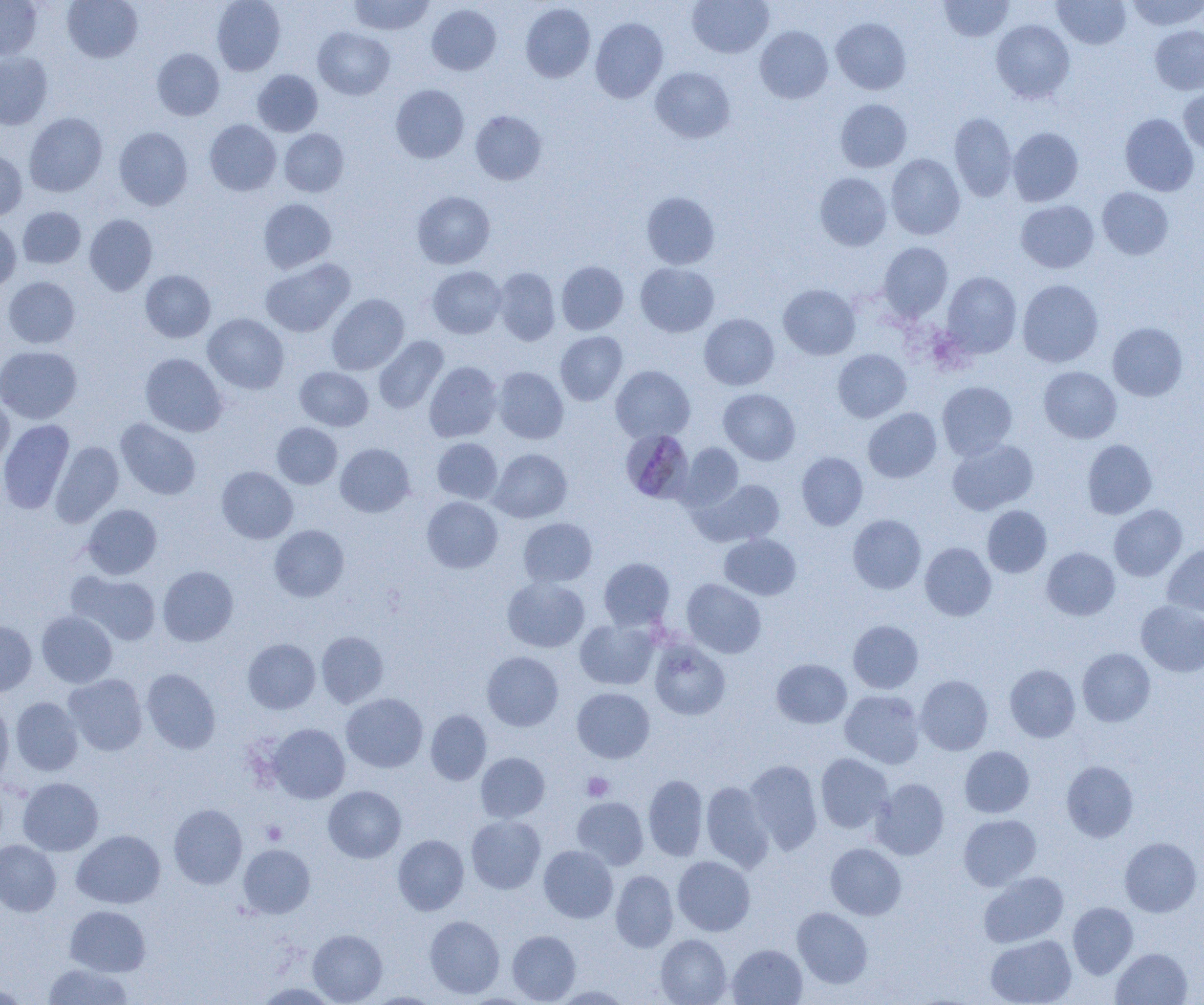

slide-level diagnosis = Plasmodium malariae
image size = 1204×1005 pixels
modality = optical microscopy
magnification = 1000x
Plasmodium malariae-infected red blood cell locations = approximate bounding boxes as [x1, y1, x2, y2] in pixels: [622, 430, 697, 502]
field of view = single
uninfected red blood cell locations = approximate bounding boxes as [x1, y1, x2, y2] in pixels: [0, 0, 42, 60], [62, 0, 142, 62], [212, 0, 286, 75], [348, 0, 434, 35], [687, 0, 773, 58], [939, 0, 1014, 42], [1053, 0, 1130, 49], [1126, 0, 1203, 32], [520, 3, 595, 83], [427, 4, 501, 76], [831, 17, 911, 94], [590, 18, 668, 103], [991, 19, 1075, 103], [755, 25, 833, 103], [1149, 25, 1204, 94], [313, 27, 394, 99], [152, 48, 224, 120], [0, 52, 53, 130], [650, 67, 735, 143], [252, 69, 323, 137], [390, 84, 469, 163], [1179, 87, 1204, 156], [835, 99, 912, 172], [470, 110, 546, 185], [24, 112, 107, 197], [949, 112, 1016, 201], [1120, 113, 1199, 196], [205, 119, 281, 196], [114, 127, 193, 210], [1008, 127, 1083, 206], [280, 129, 349, 197], [0, 150, 27, 221], [887, 153, 965, 240], [814, 172, 892, 250], [1097, 187, 1174, 260], [412, 191, 495, 269], [641, 192, 719, 269], [258, 198, 336, 273], [1016, 200, 1099, 273], [18, 207, 85, 268], [84, 214, 157, 295], [0, 219, 20, 293], [878, 242, 953, 321], [260, 258, 355, 337], [556, 261, 628, 335], [635, 262, 719, 337], [427, 266, 506, 338], [494, 268, 560, 345], [140, 270, 215, 342], [942, 271, 1021, 357], [2, 276, 80, 349], [1017, 280, 1103, 367], [778, 284, 860, 359], [327, 293, 409, 375], [203, 313, 289, 394], [699, 314, 779, 390], [1108, 322, 1187, 401], [555, 331, 628, 405], [374, 336, 448, 414], [0, 345, 82, 424], [833, 349, 911, 422], [140, 353, 227, 437], [424, 361, 502, 442], [295, 366, 373, 431], [611, 366, 695, 443], [1039, 366, 1121, 443], [494, 367, 569, 444], [937, 381, 1017, 460], [718, 389, 800, 465], [0, 396, 14, 469], [863, 408, 942, 483], [116, 418, 201, 500], [0, 420, 74, 513], [272, 422, 342, 489], [432, 438, 502, 504], [947, 439, 1038, 515], [1082, 439, 1157, 519], [51, 441, 125, 526], [335, 443, 415, 517], [677, 443, 743, 512], [490, 448, 571, 522], [797, 452, 867, 530], [217, 466, 298, 543], [694, 479, 785, 547], [422, 496, 502, 573], [82, 504, 162, 579], [1109, 504, 1187, 580], [982, 505, 1051, 577], [847, 514, 926, 594], [518, 517, 597, 587], [269, 525, 349, 602], [719, 533, 801, 601], [920, 542, 996, 621], [1162, 542, 1204, 617], [1041, 547, 1119, 620], [598, 557, 675, 630], [158, 566, 238, 646], [69, 571, 161, 645], [502, 576, 589, 652], [682, 579, 766, 658], [1136, 600, 1204, 677], [37, 610, 117, 687], [0, 619, 37, 696], [575, 619, 658, 690], [848, 620, 923, 693], [316, 631, 389, 708], [649, 637, 730, 721], [243, 638, 320, 714], [1077, 648, 1155, 726], [482, 651, 563, 731], [771, 659, 851, 728], [1005, 664, 1080, 742], [141, 668, 220, 754], [64, 674, 147, 755], [915, 675, 993, 755], [572, 687, 655, 763], [840, 690, 925, 768], [341, 693, 428, 773], [11, 697, 83, 776], [0, 698, 13, 789], [425, 710, 491, 785], [267, 723, 350, 803], [959, 746, 1034, 818], [475, 752, 549, 822], [815, 753, 893, 833], [745, 759, 822, 854], [1061, 760, 1138, 842], [643, 774, 708, 860], [18, 777, 103, 856], [871, 778, 949, 859], [701, 781, 774, 872], [323, 785, 406, 863], [572, 797, 649, 869], [169, 804, 247, 889], [959, 814, 1041, 890], [466, 815, 546, 894], [72, 830, 165, 909], [393, 834, 469, 915], [1120, 837, 1202, 917], [0, 840, 61, 916], [826, 843, 906, 919], [238, 844, 315, 918], [539, 845, 618, 923], [673, 856, 755, 936], [611, 870, 678, 952], [979, 871, 1069, 947], [1068, 902, 1138, 978], [65, 905, 150, 976], [792, 907, 872, 988], [424, 915, 504, 999], [308, 929, 387, 1004], [507, 930, 580, 1003], [656, 934, 731, 1005], [985, 935, 1076, 1005], [727, 944, 807, 1004], [1111, 948, 1192, 1005], [43, 963, 133, 1004], [0, 981, 30, 1004], [253, 982, 339, 1005], [551, 985, 632, 1004], [362, 992, 446, 1004]
platelet locations = approximate bounding boxes as [x1, y1, x2, y2] in pixels: [582, 772, 614, 802], [260, 821, 286, 845]
preparation = thin blood film